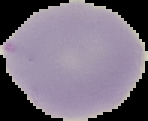

image size = 148×121 pixels
preparation = thin blood smear
malaria status = uninfected
image type = segmented cell region on a black background